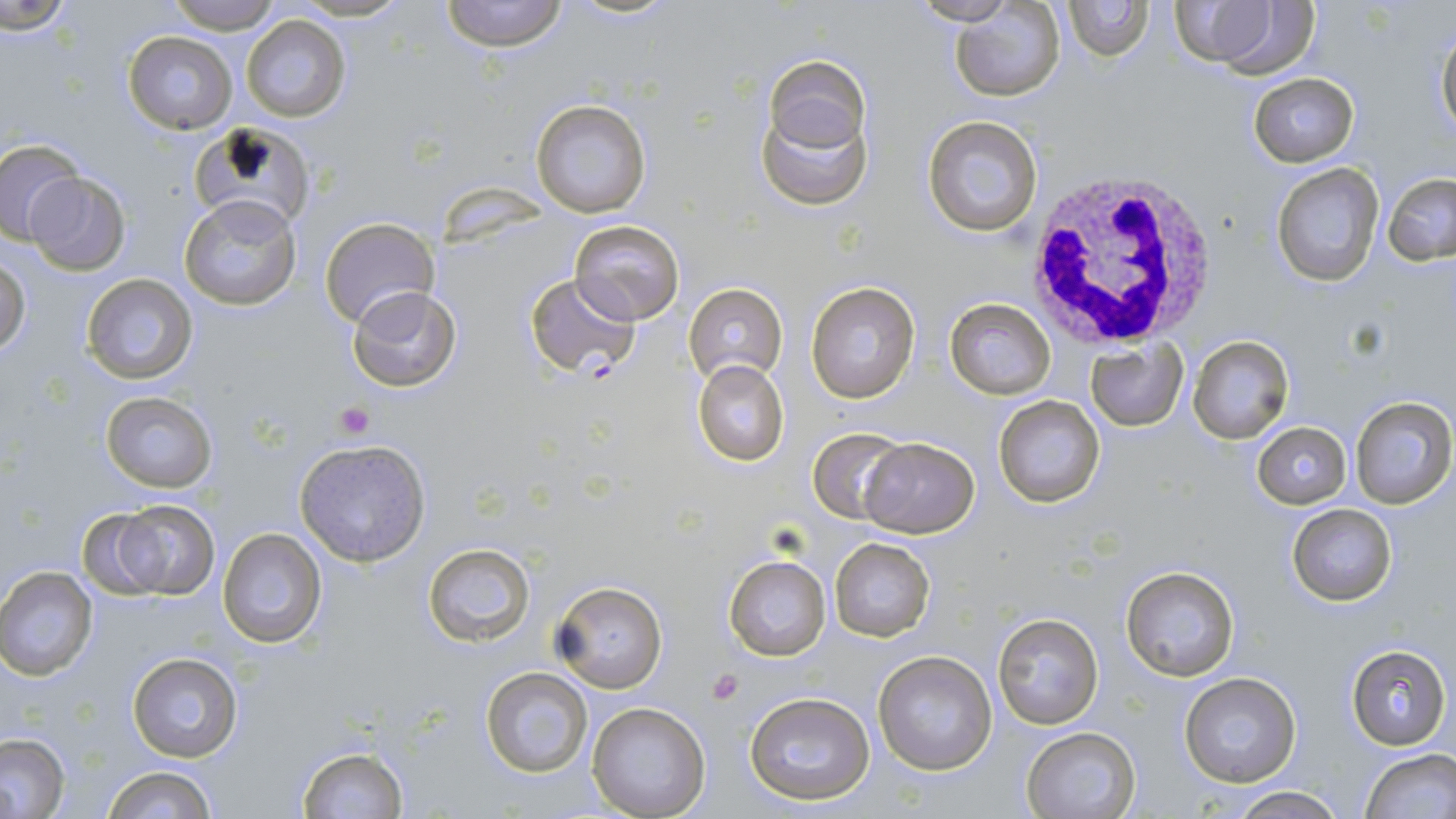

Summary:
  - Coordinate format: approximate bounding boxes as named x1/y1/x2/y2 corners in pixels
  - White blood cell locations: (x1=1020, y1=163, x2=1224, y2=349)
  - Uninfected red blood cell locations: (x1=163, y1=0, x2=283, y2=34), (x1=291, y1=0, x2=414, y2=22), (x1=440, y1=0, x2=568, y2=51), (x1=911, y1=0, x2=1020, y2=25), (x1=1062, y1=0, x2=1154, y2=61), (x1=2, y1=1, x2=80, y2=34), (x1=951, y1=2, x2=1067, y2=102), (x1=1169, y1=3, x2=1318, y2=78), (x1=242, y1=14, x2=349, y2=122), (x1=1435, y1=25, x2=1456, y2=144), (x1=125, y1=31, x2=238, y2=132), (x1=765, y1=57, x2=872, y2=159), (x1=1246, y1=73, x2=1360, y2=166), (x1=755, y1=84, x2=873, y2=211), (x1=530, y1=100, x2=651, y2=219), (x1=922, y1=114, x2=1043, y2=238), (x1=186, y1=120, x2=315, y2=237), (x1=0, y1=138, x2=83, y2=246), (x1=1270, y1=164, x2=1384, y2=286), (x1=22, y1=172, x2=131, y2=275), (x1=1382, y1=173, x2=1456, y2=267), (x1=180, y1=196, x2=302, y2=311), (x1=319, y1=216, x2=439, y2=330), (x1=569, y1=219, x2=684, y2=326), (x1=0, y1=257, x2=29, y2=357), (x1=81, y1=274, x2=197, y2=385), (x1=806, y1=281, x2=920, y2=403), (x1=683, y1=283, x2=788, y2=384), (x1=345, y1=284, x2=462, y2=393), (x1=944, y1=298, x2=1056, y2=399), (x1=1188, y1=336, x2=1295, y2=443), (x1=1085, y1=341, x2=1186, y2=432), (x1=692, y1=359, x2=790, y2=466), (x1=99, y1=391, x2=218, y2=492), (x1=993, y1=395, x2=1107, y2=508), (x1=1350, y1=395, x2=1455, y2=509), (x1=1250, y1=421, x2=1353, y2=508), (x1=809, y1=428, x2=908, y2=524), (x1=858, y1=438, x2=979, y2=538), (x1=294, y1=440, x2=431, y2=567), (x1=104, y1=499, x2=221, y2=600), (x1=1286, y1=504, x2=1398, y2=605), (x1=217, y1=528, x2=327, y2=647), (x1=829, y1=539, x2=935, y2=641), (x1=422, y1=542, x2=537, y2=646), (x1=723, y1=555, x2=831, y2=661), (x1=1119, y1=566, x2=1240, y2=681), (x1=0, y1=567, x2=98, y2=679), (x1=551, y1=578, x2=669, y2=694), (x1=991, y1=610, x2=1106, y2=731), (x1=1346, y1=645, x2=1450, y2=749), (x1=874, y1=650, x2=999, y2=776), (x1=126, y1=652, x2=243, y2=764), (x1=479, y1=667, x2=596, y2=779), (x1=1178, y1=673, x2=1301, y2=788), (x1=744, y1=691, x2=876, y2=807), (x1=587, y1=700, x2=712, y2=819), (x1=1021, y1=727, x2=1140, y2=818), (x1=0, y1=735, x2=71, y2=816), (x1=296, y1=746, x2=409, y2=818), (x1=1359, y1=748, x2=1456, y2=819), (x1=101, y1=764, x2=217, y2=819), (x1=1224, y1=786, x2=1347, y2=819)
  - Plasmodium falciparum-infected red blood cell locations: (x1=524, y1=273, x2=640, y2=379)
  - Platelet locations: (x1=335, y1=404, x2=372, y2=440), (x1=706, y1=667, x2=743, y2=705)
  - Slide-level diagnosis: Plasmodium falciparum
  - Field of view: single
  - Preparation: thin blood film
  - Modality: light microscopy
  - Image size: 1456×819 pixels
  - Magnification: 1000x
  - Stain: May-Grünwald-Giemsa